Name the blood parasite species.
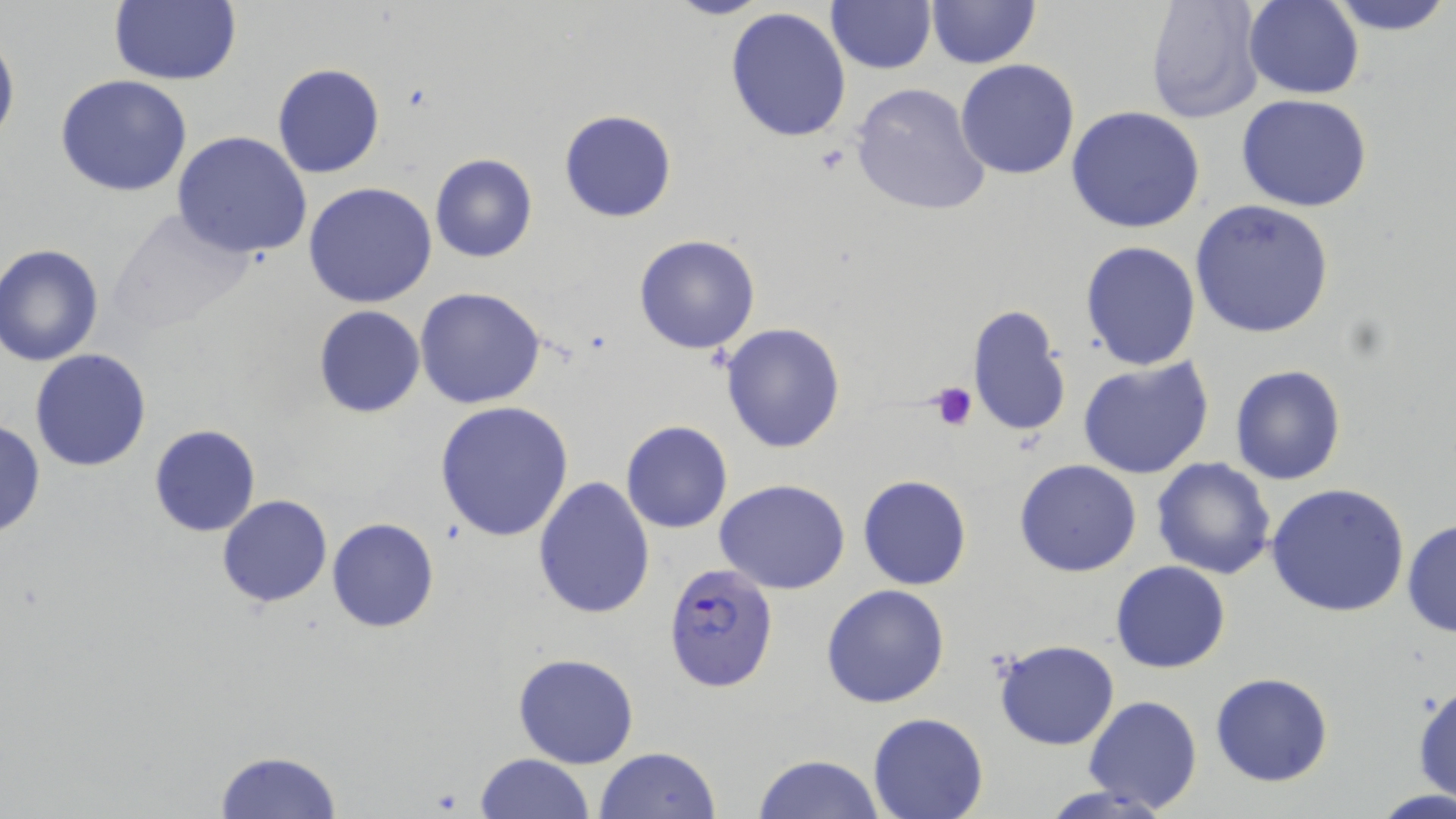

Plasmodium falciparum.

modality = optical microscopy
magnification = 1000x
preparation = thin blood film
Plasmodium falciparum-infected red blood cell locations = approximate bounding boxes as named x1/y1/x2/y2 corners in pixels: (x1=663, y1=563, x2=779, y2=690)
stain = May-Grünwald-Giemsa
image size = 1456×819 pixels
uninfected red blood cell locations = approximate bounding boxes as named x1/y1/x2/y2 corners in pixels: (x1=108, y1=0, x2=241, y2=86), (x1=663, y1=0, x2=775, y2=21), (x1=925, y1=0, x2=1039, y2=69), (x1=1145, y1=0, x2=1265, y2=125), (x1=1322, y1=0, x2=1454, y2=37), (x1=826, y1=1, x2=935, y2=74), (x1=1243, y1=1, x2=1364, y2=99), (x1=725, y1=6, x2=853, y2=145), (x1=0, y1=27, x2=19, y2=154), (x1=954, y1=59, x2=1080, y2=180), (x1=271, y1=62, x2=384, y2=178), (x1=55, y1=74, x2=193, y2=197), (x1=849, y1=82, x2=992, y2=217), (x1=1235, y1=93, x2=1372, y2=211), (x1=1065, y1=106, x2=1206, y2=232), (x1=557, y1=109, x2=677, y2=224), (x1=171, y1=131, x2=313, y2=261), (x1=429, y1=153, x2=538, y2=264), (x1=304, y1=182, x2=437, y2=308), (x1=1190, y1=200, x2=1334, y2=338), (x1=102, y1=208, x2=264, y2=338), (x1=633, y1=234, x2=761, y2=355), (x1=1080, y1=241, x2=1202, y2=371), (x1=0, y1=243, x2=104, y2=366), (x1=415, y1=287, x2=548, y2=409), (x1=313, y1=304, x2=426, y2=418), (x1=964, y1=304, x2=1073, y2=438), (x1=720, y1=321, x2=848, y2=453), (x1=30, y1=349, x2=151, y2=471), (x1=1079, y1=357, x2=1215, y2=480), (x1=1230, y1=365, x2=1347, y2=485), (x1=434, y1=401, x2=574, y2=542), (x1=1, y1=418, x2=47, y2=539), (x1=620, y1=420, x2=734, y2=534), (x1=148, y1=425, x2=261, y2=537), (x1=1150, y1=456, x2=1277, y2=580), (x1=1013, y1=458, x2=1142, y2=577), (x1=532, y1=474, x2=656, y2=620), (x1=858, y1=474, x2=971, y2=590), (x1=849, y1=475, x2=964, y2=705), (x1=715, y1=478, x2=851, y2=595), (x1=1265, y1=483, x2=1410, y2=618), (x1=216, y1=495, x2=333, y2=608), (x1=326, y1=517, x2=439, y2=634), (x1=1402, y1=519, x2=1456, y2=637), (x1=1110, y1=561, x2=1231, y2=673), (x1=821, y1=584, x2=950, y2=708), (x1=992, y1=639, x2=1120, y2=751), (x1=512, y1=652, x2=640, y2=770), (x1=1209, y1=674, x2=1333, y2=788), (x1=1411, y1=683, x2=1456, y2=796), (x1=1081, y1=695, x2=1203, y2=813), (x1=867, y1=713, x2=989, y2=819), (x1=594, y1=747, x2=722, y2=818), (x1=214, y1=748, x2=341, y2=818), (x1=474, y1=753, x2=596, y2=818), (x1=754, y1=753, x2=884, y2=819), (x1=1038, y1=783, x2=1178, y2=819), (x1=1371, y1=790, x2=1454, y2=817)
platelet locations = approximate bounding boxes as named x1/y1/x2/y2 corners in pixels: (x1=929, y1=382, x2=978, y2=431)
field of view = one of a larger specimen